Assess this cell for malaria.
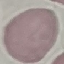

Uninfected.

Giemsa stain. Thin blood smear. Automatically extracted cell patch, resized to 64 × 64 pixels. Photographed with a smartphone camera at the microscope eyepiece.